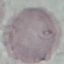
result = no malaria parasites detected
capture = smartphone through the microscope eyepiece
image type = cell patch, automatically extracted from a larger field of view and resized to 64 × 64 pixels
preparation = thin blood smear
stain = Giemsa